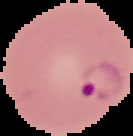
Image is 133×136 pixels. Segmented cell region on a black background. Result: Plasmodium parasites identified. From a thin blood smear.